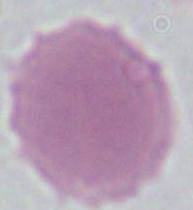
Photomicrograph. 1000x magnification. An erythrocyte is seen.